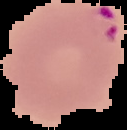 From a thin blood film. Result: malaria parasites detected. The area outside the segmented cell region is set to black. Image is 127×130 pixels.